Name the cell type shown.
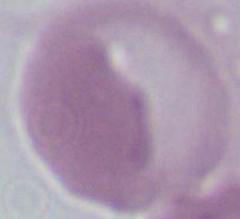
An erythrocyte.

Micrograph. 1000x magnification.